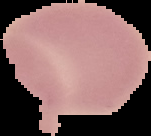
Summary:
  - Image size: 151×136 pixels
  - Preparation: thin blood smear
  - Image type: segmented cell region on a black background
  - Malaria status: uninfected